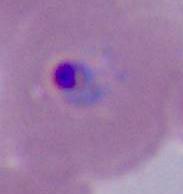

modality = photomicrograph
identification = Plasmodium
magnification = 400x or 1000x